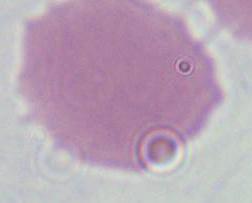

Summary:
  - Identification: red blood cell
  - Modality: photomicrograph
  - Magnification: 1000x